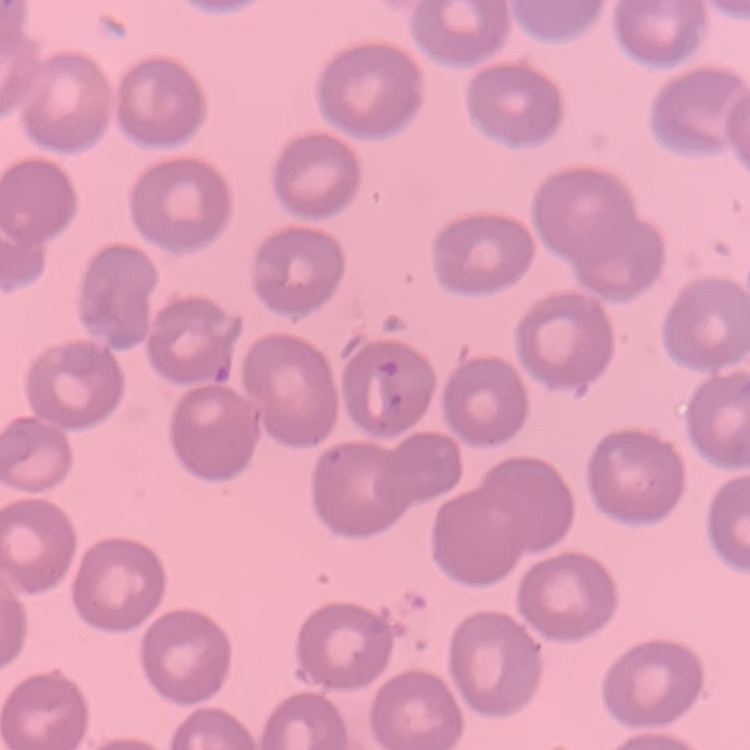
Summary:
  - Erythrocyte morphology: no rouleaux formation
  - Image type: one tile cut from a larger photomicrograph
  - Stain: Field's or Giemsa
  - Preparation: thin blood smear